Assess this cell for malaria.
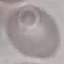

Uninfected.

Cell patch, automatically extracted from a larger field of view and resized to 64 × 64 pixels. Giemsa-stained preparation. Thin blood film. Photographed with a smartphone camera at the microscope eyepiece.